Outline each blood parasite and name the species.
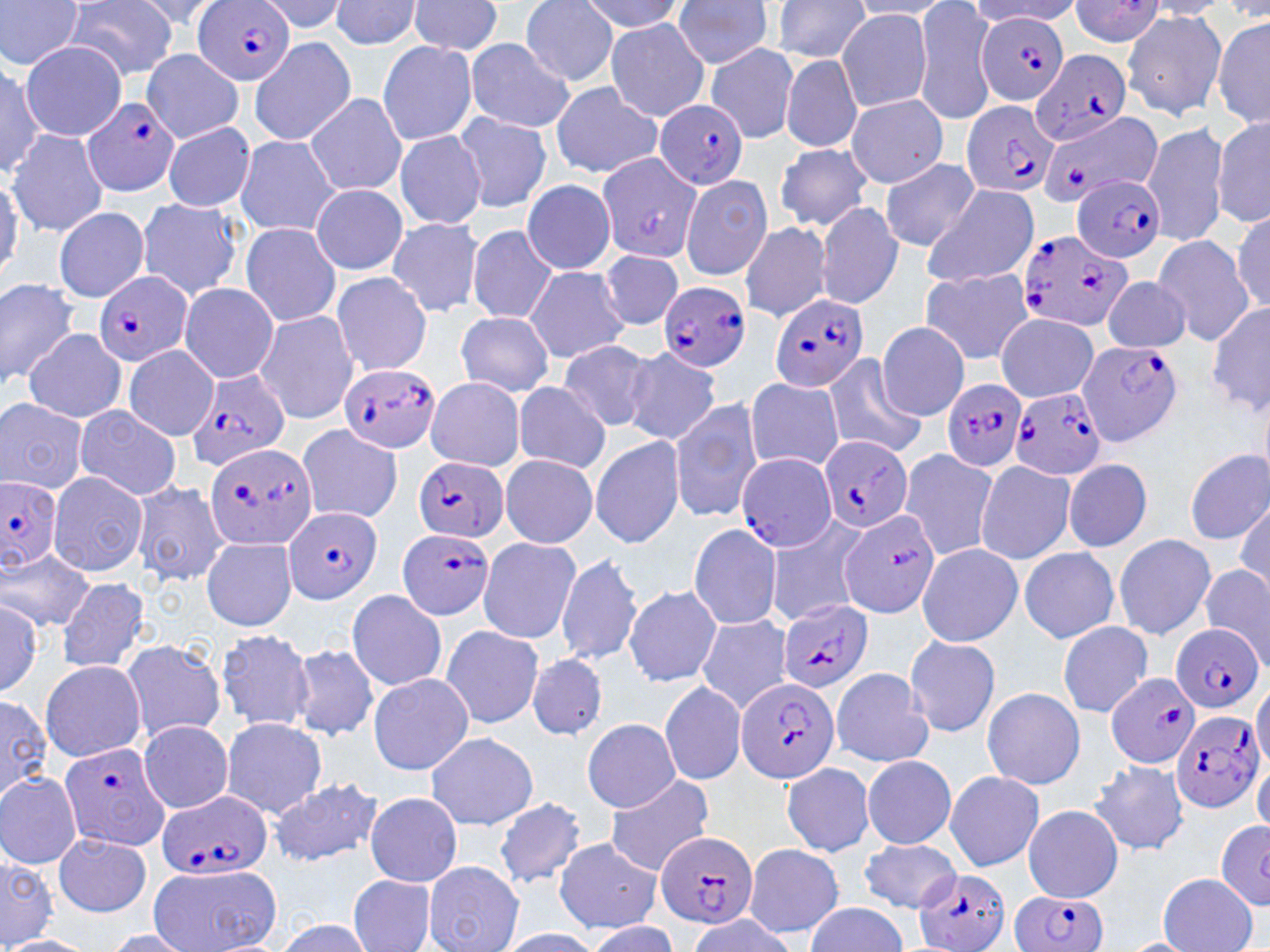

Approximate bounding boxes as (x1,y1)-(x2,y2) corner pairs in pixels.
Plasmodium falciparum-infected red blood cells: (195,0)-(296,87), (978,13)-(1070,105), (1028,50)-(1131,148), (83,96)-(183,197), (960,101)-(1058,199), (656,102)-(748,189), (1039,114)-(1166,208), (1074,174)-(1166,264), (1015,228)-(1129,334), (94,271)-(193,368), (658,280)-(753,373), (768,293)-(869,394), (1077,338)-(1185,445), (337,362)-(443,452), (187,367)-(291,471), (942,379)-(1026,471), (1008,387)-(1108,482), (818,435)-(913,534), (201,442)-(319,552), (733,451)-(837,553), (414,456)-(508,544), (0,476)-(63,574), (284,506)-(382,605), (399,528)-(497,621), (776,600)-(874,695), (1170,623)-(1263,713), (1107,671)-(1201,769), (735,676)-(838,785), (1169,709)-(1265,814), (58,742)-(170,851), (155,790)-(273,881), (657,829)-(758,932), (913,868)-(1011,952), (1009,891)-(1112,952).
No Plasmodium ovale, Plasmodium malariae, Plasmodium vivax, Babesia divergens, or Trypanosoma brucei observed.

Uninfected red blood cell locations: (126,0)-(226,33), (256,0)-(349,34), (329,0)-(424,51), (406,0)-(505,58), (520,0)-(620,86), (579,0)-(686,34), (672,0)-(777,71), (1068,0)-(1167,44), (0,1)-(86,69), (65,1)-(179,81), (768,1)-(871,62), (849,1)-(953,20), (1140,1)-(1231,19), (914,2)-(997,124), (968,2)-(1085,25), (1121,9)-(1227,121), (837,10)-(933,111), (1213,15)-(1269,132), (605,18)-(709,121), (249,37)-(356,145), (464,38)-(575,133), (21,40)-(126,139), (376,41)-(477,145), (706,42)-(800,145), (140,49)-(245,142), (780,54)-(861,153), (0,60)-(46,176), (548,83)-(663,178), (846,93)-(949,188), (306,94)-(407,198), (454,112)-(550,213), (1211,118)-(1270,228), (163,121)-(257,212), (1141,122)-(1232,247), (6,129)-(106,236), (393,130)-(486,230), (233,135)-(342,237), (774,144)-(873,231), (595,152)-(701,269), (880,158)-(979,252), (680,173)-(773,282), (0,176)-(25,282), (521,183)-(616,276), (923,183)-(1040,287), (311,185)-(409,274), (134,196)-(243,301), (814,200)-(904,309), (53,206)-(151,303), (1233,209)-(1270,313), (386,217)-(484,317), (739,220)-(832,323), (241,223)-(343,328), (466,224)-(560,325), (1152,237)-(1253,346), (597,250)-(685,332), (523,267)-(630,364), (918,268)-(1034,365), (329,272)-(434,376), (1102,274)-(1192,353), (0,276)-(80,387), (178,283)-(279,383), (1208,300)-(1270,417), (254,309)-(359,425), (456,312)-(555,396), (997,314)-(1098,401), (877,321)-(970,421), (23,330)-(128,423), (556,339)-(659,433), (123,344)-(218,440), (621,346)-(721,445), (821,354)-(927,460), (426,376)-(526,472), (744,377)-(845,473), (513,381)-(611,473), (669,397)-(763,522), (0,398)-(89,494), (73,405)-(183,502), (688,424)-(808,547), (293,425)-(405,524), (591,435)-(686,548), (1183,447)-(1270,545), (896,448)-(996,560), (500,454)-(597,547), (1061,457)-(1155,554), (975,460)-(1077,565), (47,471)-(148,578), (130,480)-(230,586), (1234,497)-(1270,595), (838,510)-(940,618), (764,515)-(867,626), (688,522)-(784,630), (1113,533)-(1216,641), (476,536)-(580,644), (198,537)-(296,631), (916,542)-(1023,647), (1019,548)-(1120,643), (1,551)-(95,629), (555,554)-(643,664), (1199,566)-(1270,663), (55,576)-(153,675), (623,584)-(722,685), (346,589)-(448,691), (0,596)-(43,697), (695,615)-(793,714), (1057,621)-(1153,717), (440,624)-(544,729), (215,628)-(317,731), (905,635)-(1001,738), (118,638)-(226,744), (290,645)-(380,742), (527,653)-(607,739), (38,659)-(147,762), (830,667)-(933,768), (368,673)-(474,775), (1251,675)-(1270,776), (659,680)-(747,786), (981,686)-(1085,790), (0,695)-(50,801), (220,717)-(327,819), (582,719)-(682,812), (138,720)-(234,811), (424,731)-(539,831), (862,755)-(957,849), (1253,755)-(1270,840), (781,761)-(877,858), (1089,761)-(1191,852), (943,770)-(1045,871), (0,772)-(82,869), (603,775)-(715,875), (268,778)-(383,868), (365,791)-(462,887), (496,798)-(586,887), (1022,805)-(1123,902), (1216,818)-(1270,908), (52,832)-(151,918), (860,838)-(960,912), (552,839)-(662,934), (741,841)-(844,937), (0,851)-(57,946), (423,861)-(524,952), (150,864)-(282,952), (1157,872)-(1258,952), (346,873)-(438,952), (804,901)-(910,951), (681,915)-(801,951), (273,917)-(377,952), (581,921)-(679,952), (497,928)-(605,951), (100,929)-(201,951), (3,936)-(96,952), (1116,937)-(1201,952). Slide-level diagnosis: Plasmodium falciparum. Captured at 1000x magnification. Image is 1270×952 pixels. Thin blood film. Single field of view. Light microscopy. May-Grünwald-Giemsa stain.